Report the malaria status of this cell.
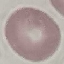
Uninfected.

Giemsa stain. Photographed with a smartphone camera at the microscope eyepiece. Thin blood film. Cell patch, automatically extracted from a larger field of view and resized to 64 × 64 pixels.